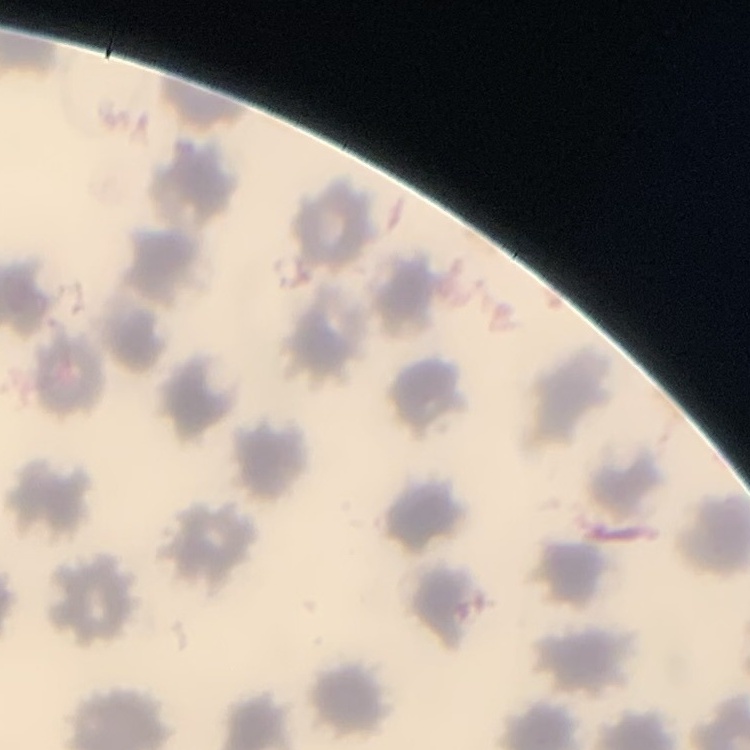

red_blood_cell_morphology: no rouleaux formation
image_type: one tile cut from a larger photomicrograph
stain: Field's or Giemsa
preparation: thin blood smear